Assess this cell for malaria.
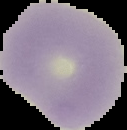

Uninfected.

From a thin blood film. Segmented cell region on a black background. Image is 127×130 pixels.